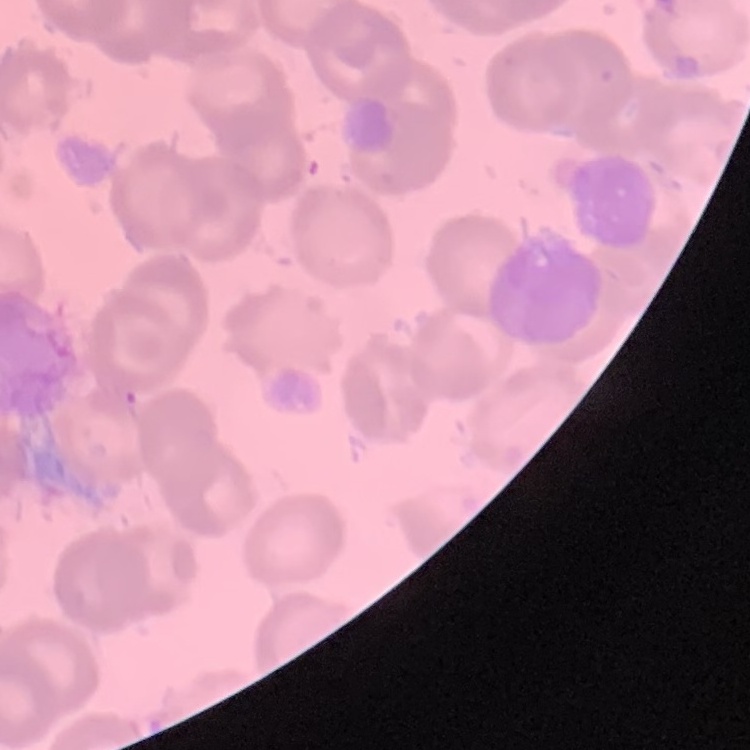
Summary:
  - Red blood cell morphology: no rouleaux formation
  - Stain: Field's or Giemsa
  - Image type: one tile cut from a larger photomicrograph
  - Preparation: thin blood film